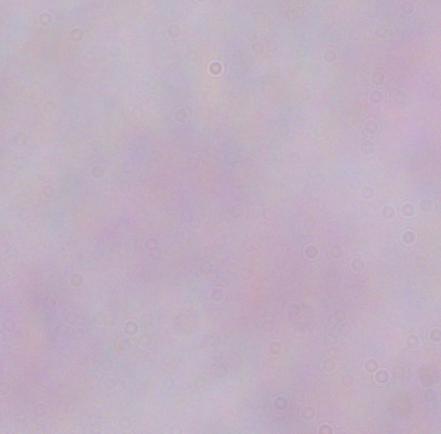

{
  "magnification": "1000x",
  "identification": "trypanosome",
  "modality": "photomicrograph"
}